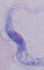
A trypanosome is shown. Captured at 1000x magnification. Photomicrograph.